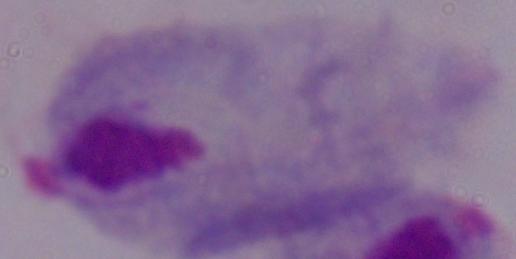 1000x magnification. Micrograph. A trichomonad is shown.